Assess this cell for malaria.
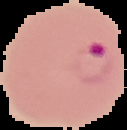
It is parasitized.

Image is 127×130 pixels. Cell region segmented out of the field of view; the surrounding area is masked to black. From a thin blood film.